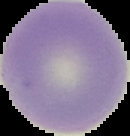 Image is 130×136 pixels. Result: no Plasmodium parasites seen. The area outside the segmented cell region is set to black. From a thin blood smear.